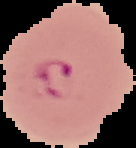

image type = segmented cell region with the area outside set to black
image size = 136×148 pixels
preparation = thin blood smear
malaria status = parasitized